State which parasite is depicted.
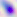

This is Toxoplasma gondii.

400x magnification. Micrograph.